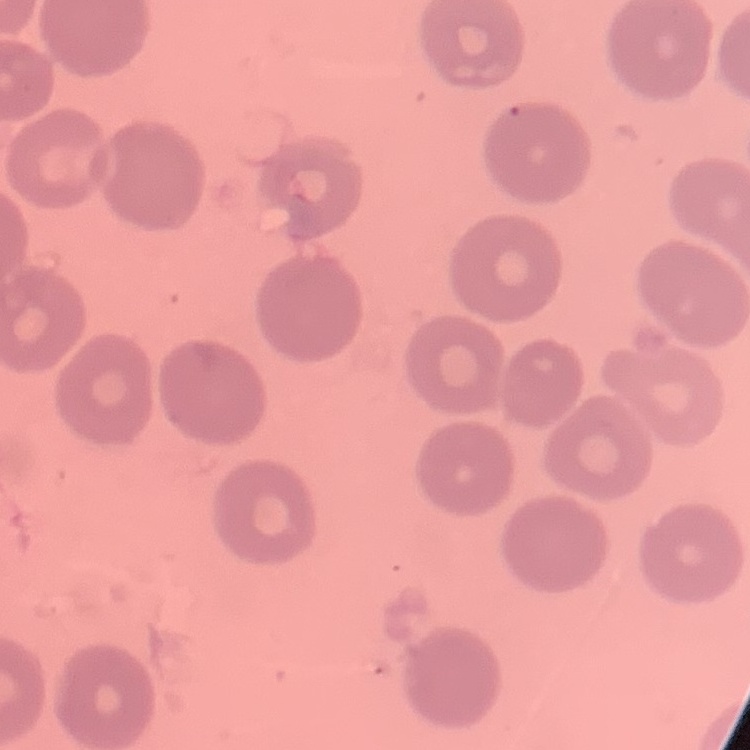

erythrocyte morphology = no rouleaux formation
stain = Field's or Giemsa
preparation = thin peripheral smear
image type = square crop of a larger photomicrograph